Assess the morphology of the erythrocytes.
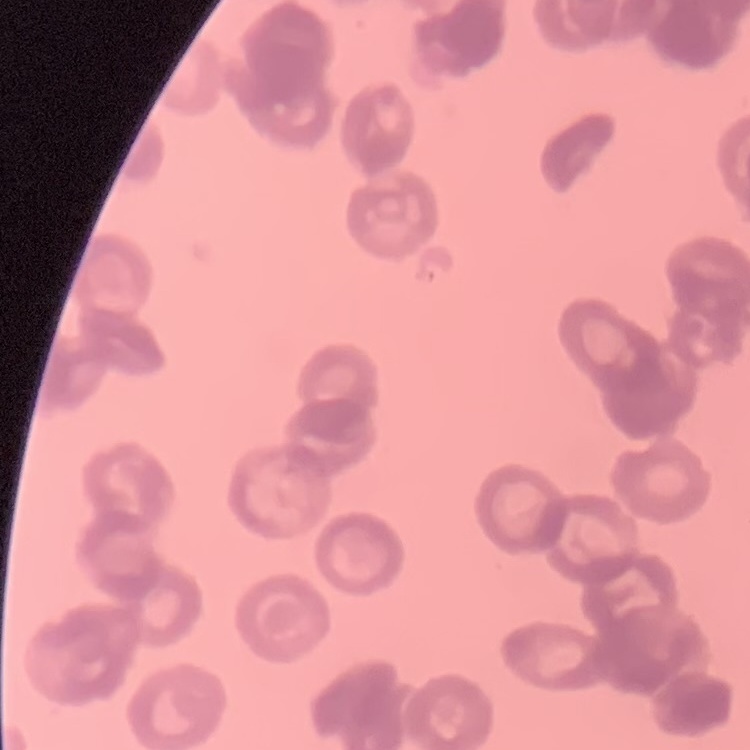
They show rouleaux formation.

One tile cut from a larger photomicrograph. Thin peripheral smear. Field's or Giemsa stain.